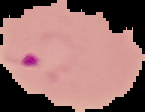
preparation: thin blood smear
malaria_status: parasitized
image_size: 145×112 pixels
image_type: segmented cell region with the area outside set to black